Identify the preparation type.
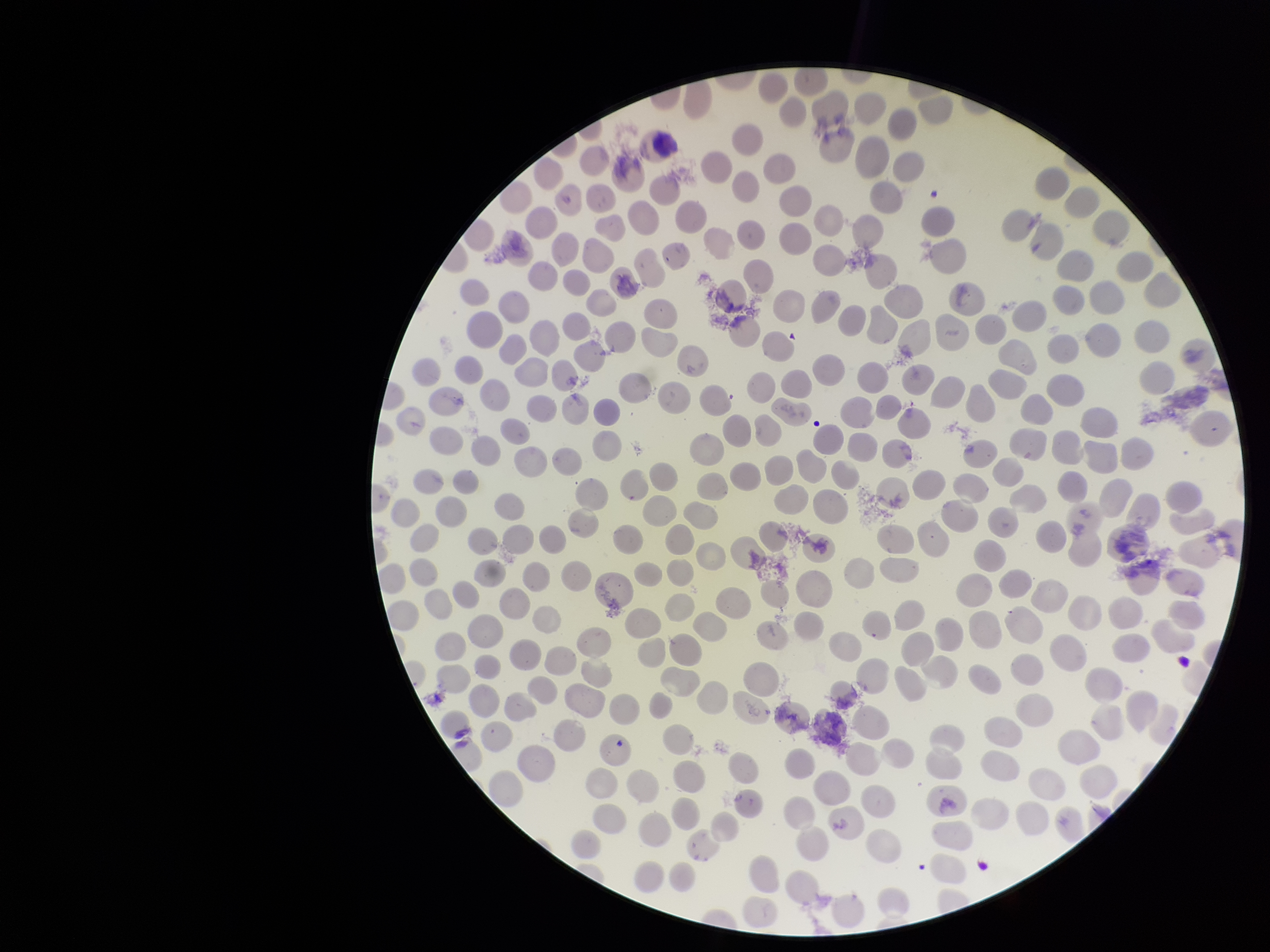
Thin.

Summary:
  - Field of view: one from this slide
  - Parasitized red blood cell count: 0
  - Red blood cell count: 237
  - Species reported for this patient: Plasmodium vivax
  - Parasitized red blood cells: none identified
  - Stain: Giemsa
  - Capture: smartphone photograph through the microscope eyepiece
  - Patient malaria status: positive
  - Image size: 1270×952 pixels